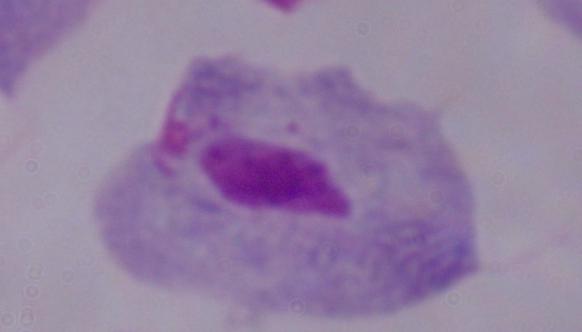

Summary:
  - Magnification: 1000x
  - Modality: micrograph
  - Identification: trichomonad